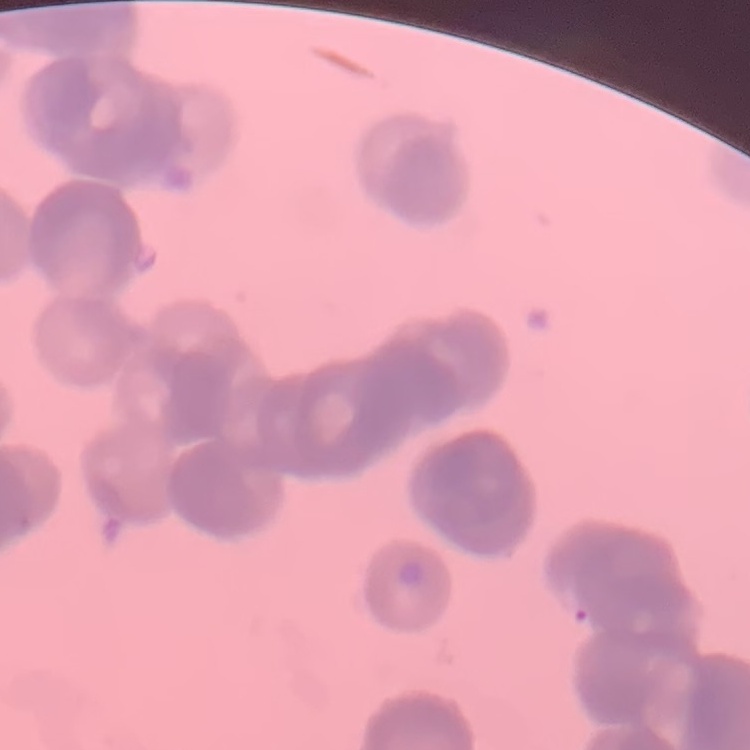 The red blood cells show rouleaux formation. Thin blood film. Square crop of a larger photomicrograph. Field's or Giemsa stain.